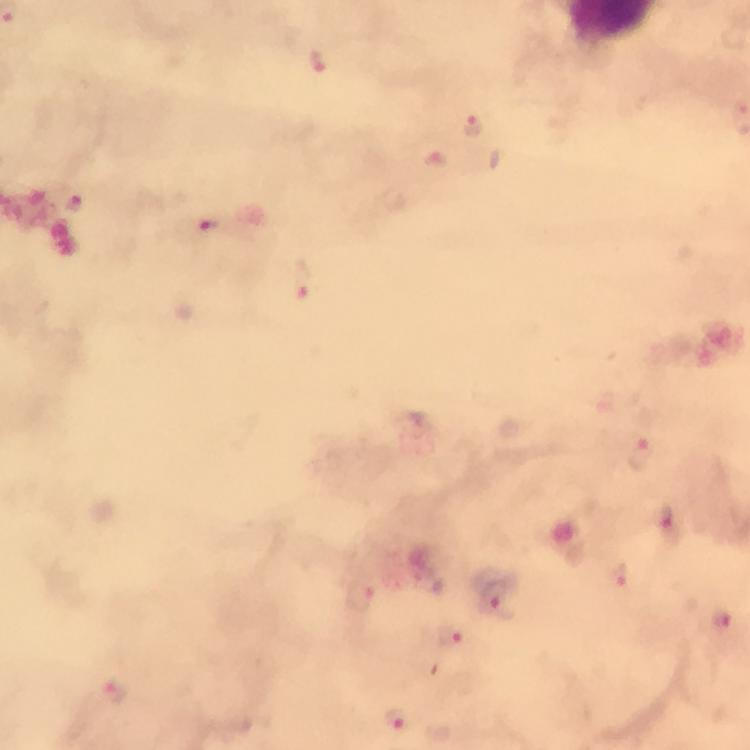
Approximate object centers, in pixels from the top-left corner. Plasmodium parasite locations: (x=316, y=58), (x=476, y=126), (x=74, y=202), (x=207, y=225), (x=300, y=283), (x=640, y=454), (x=669, y=522), (x=620, y=573), (x=363, y=596), (x=496, y=600), (x=722, y=619), (x=452, y=637), (x=116, y=694), (x=399, y=717). A crop from one field of view. Image is 750×750 pixels. Thick smear. Immersion oil applied. Photographed through the microscope with a smartphone camera. At 100x magnification. From a diagnostic examination for malaria. Giemsa stain.